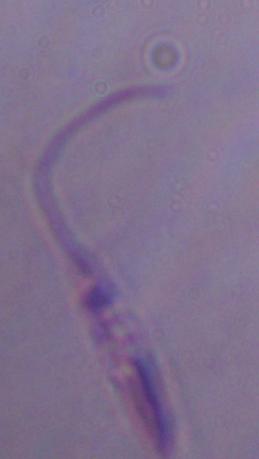

Summary:
  - Identification: Leishmania
  - Modality: photomicrograph
  - Magnification: 1000x